Point out each Plasmodium parasite and each leukocyte.
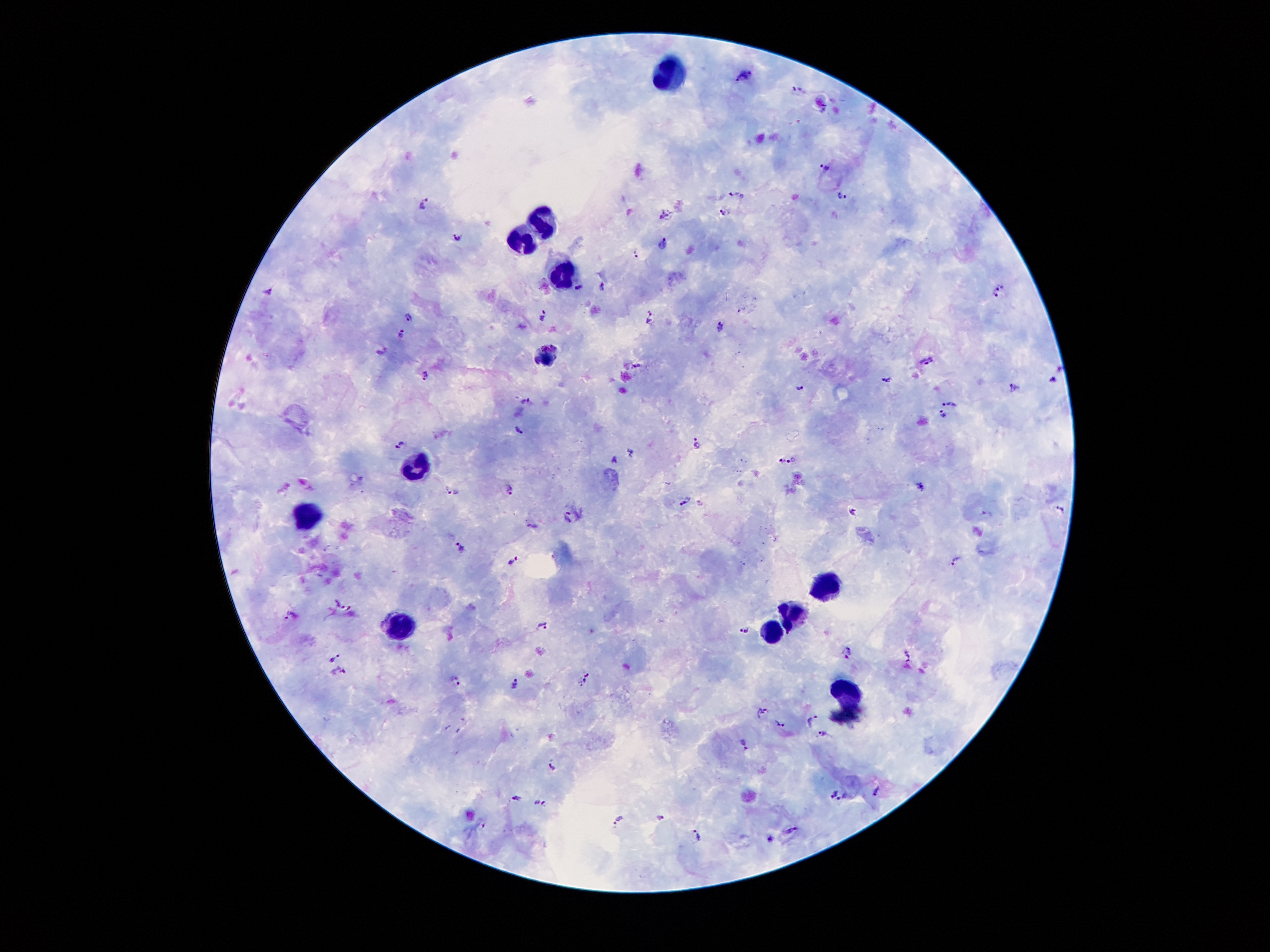

Approximate object centers, in pixels from the top-left corner.
Plasmodium parasites: (x=743, y=75), (x=795, y=89), (x=825, y=167), (x=737, y=195), (x=842, y=195), (x=424, y=202), (x=724, y=213), (x=664, y=216), (x=457, y=238), (x=663, y=244), (x=635, y=254), (x=602, y=286), (x=580, y=287), (x=1000, y=288), (x=267, y=291), (x=993, y=296), (x=741, y=310), (x=650, y=316), (x=543, y=317), (x=408, y=318), (x=719, y=325), (x=402, y=333), (x=549, y=344), (x=383, y=351), (x=928, y=360), (x=535, y=361), (x=636, y=367), (x=425, y=376), (x=1055, y=378), (x=887, y=381), (x=800, y=387), (x=1015, y=388), (x=527, y=402), (x=948, y=402), (x=943, y=416), (x=517, y=430), (x=697, y=443), (x=399, y=445), (x=614, y=459), (x=779, y=460), (x=792, y=460), (x=920, y=486), (x=508, y=487), (x=454, y=491), (x=686, y=500), (x=1061, y=508), (x=852, y=512), (x=988, y=514), (x=568, y=516), (x=462, y=548), (x=513, y=560), (x=956, y=561), (x=340, y=603), (x=289, y=614), (x=544, y=626), (x=745, y=630), (x=846, y=653), (x=908, y=656), (x=334, y=659), (x=340, y=672), (x=586, y=679), (x=457, y=681), (x=514, y=684), (x=760, y=711), (x=812, y=722), (x=781, y=725), (x=822, y=733), (x=745, y=745), (x=554, y=767), (x=877, y=791), (x=832, y=792), (x=845, y=797), (x=519, y=799), (x=539, y=803), (x=661, y=817), (x=620, y=820), (x=483, y=825), (x=792, y=829), (x=697, y=835), (x=772, y=839).
Leukocytes: (x=664, y=75), (x=548, y=226), (x=525, y=236), (x=563, y=278), (x=416, y=462), (x=306, y=514), (x=829, y=588), (x=791, y=613), (x=397, y=623), (x=771, y=631), (x=847, y=689).

{
  "magnification": "100x",
  "field_of_view": "single",
  "capture": "smartphone camera through the microscope eyepiece",
  "preparation": "thick blood film",
  "stain": "Giemsa",
  "patient_malaria_status": "infected with Plasmodium falciparum",
  "image_size": "1270×952 pixels"
}